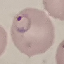 Result: malaria parasites detected. Thin blood film. Giemsa stain. Acquired by smartphone through the microscope eyepiece. Automatically extracted cell patch, resized to 64 × 64 pixels.